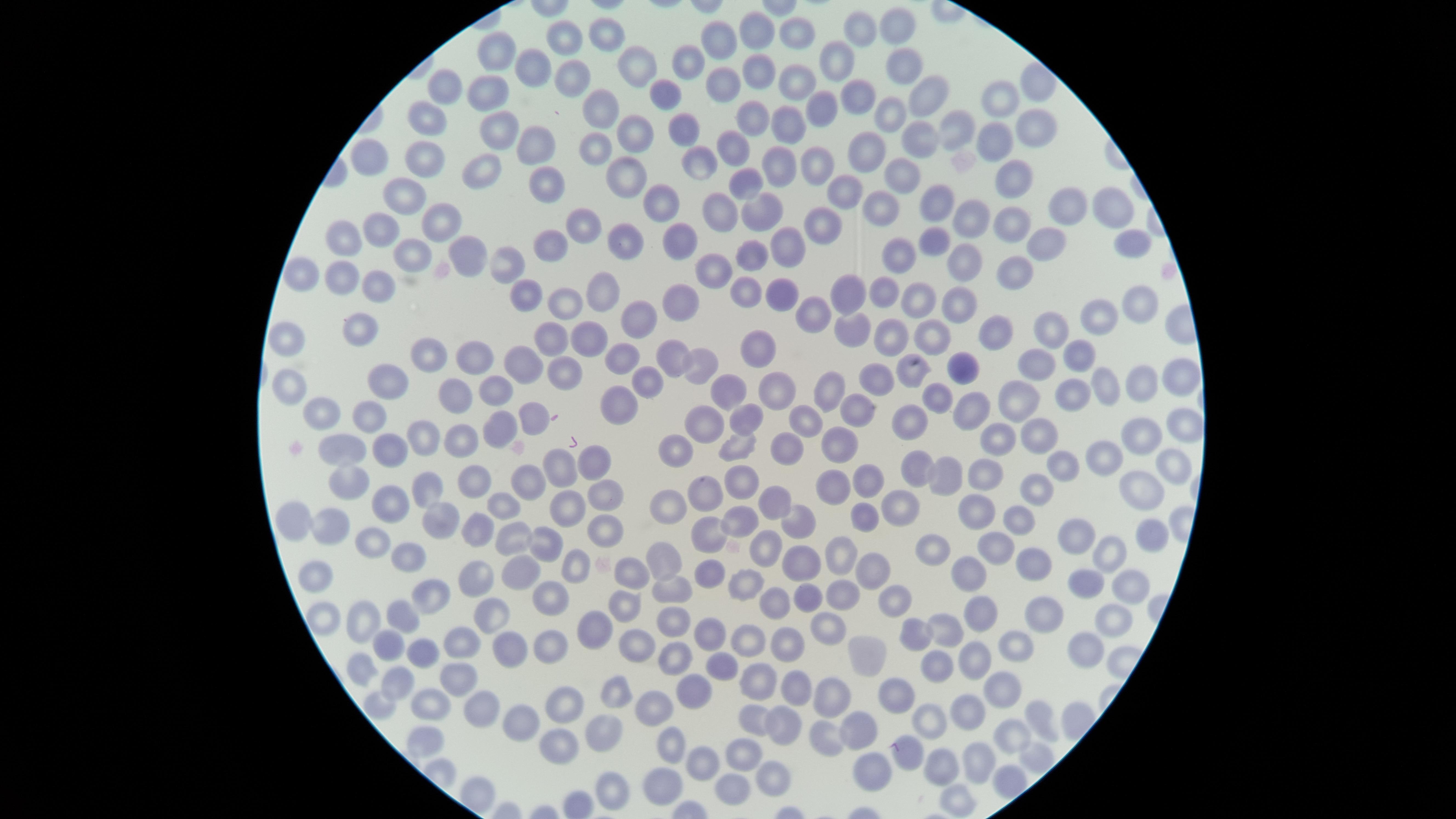
Approximate marker points as [x, y] in pixels.
Summary:
  - Uninfected RBCs: [861, 28], [901, 29], [608, 31], [800, 32], [755, 34], [567, 35], [721, 42], [500, 54], [691, 56], [838, 59], [642, 64], [900, 64], [531, 70], [758, 70], [569, 79], [799, 79], [721, 82], [452, 86], [492, 86], [931, 87], [664, 88], [855, 96], [1002, 103], [596, 108], [821, 111], [430, 116], [752, 118], [889, 118], [681, 125], [790, 125], [960, 126], [496, 128], [637, 130], [1033, 130], [918, 137], [532, 138], [593, 144], [1000, 144], [731, 145], [867, 154], [696, 155], [379, 156], [424, 156], [818, 160], [778, 165], [898, 169], [629, 174], [1009, 175], [486, 176], [548, 185], [744, 185], [851, 192], [402, 195], [661, 202], [715, 206], [879, 206], [1062, 206], [1111, 208], [758, 210], [930, 211], [443, 217], [584, 218], [973, 218], [388, 220], [819, 222], [1016, 224], [548, 237], [624, 237], [336, 240], [790, 241], [683, 244], [932, 246], [1048, 246], [1127, 247], [473, 249], [759, 252], [411, 261], [903, 261], [507, 263], [966, 264], [1017, 269], [709, 270], [304, 271], [375, 276], [344, 279], [601, 287], [783, 289], [747, 290], [885, 290], [563, 294], [530, 296], [917, 299], [683, 301], [851, 301], [963, 305], [1132, 305], [815, 316], [642, 319], [1105, 319], [893, 325], [854, 327], [989, 328], [1051, 330], [553, 331], [363, 332], [590, 334], [930, 337], [285, 341], [758, 347], [425, 348], [1080, 356], [476, 359], [521, 360], [676, 362], [622, 363], [701, 366], [561, 368], [1033, 368], [913, 372], [960, 372], [1175, 374], [878, 378], [1141, 383], [389, 384], [288, 386], [1109, 388], [645, 389], [495, 390], [780, 390], [1073, 391], [823, 392], [720, 396], [937, 398], [1019, 399], [451, 404], [617, 405], [324, 408], [968, 410], [855, 411], [372, 412], [523, 412], [912, 415], [747, 418], [806, 421], [699, 422], [498, 428], [1182, 428], [421, 430], [1040, 431], [1143, 438], [1002, 439], [737, 443], [346, 445], [840, 445], [456, 446], [790, 449], [394, 450], [677, 450], [1108, 453], [601, 460], [914, 465], [1168, 466], [1056, 467], [567, 468], [985, 469], [949, 477], [475, 480], [525, 481], [870, 481], [345, 482], [737, 486], [840, 488], [1031, 488], [1137, 488], [424, 491], [604, 492], [706, 492], [567, 500], [388, 501], [666, 503], [775, 504], [503, 505], [897, 507], [978, 509], [864, 512], [286, 517], [434, 519], [598, 519], [475, 520], [733, 520], [1017, 521], [330, 527], [800, 529], [509, 533], [1148, 535], [1071, 537], [370, 539], [707, 539], [543, 546], [841, 549], [927, 549], [995, 550], [764, 551], [403, 552], [1108, 553], [665, 561], [576, 562], [798, 563], [1030, 565], [873, 567], [978, 570], [316, 571], [514, 571], [632, 572], [709, 573], [475, 577], [1087, 579], [1128, 580], [746, 587], [669, 590], [843, 592], [429, 595], [549, 597], [813, 599], [779, 604], [896, 604], [625, 605], [1032, 605], [486, 612], [989, 614], [1111, 614], [401, 615], [671, 618], [324, 619], [835, 621], [364, 624], [591, 628], [949, 629], [712, 630], [911, 630], [748, 639], [784, 639], [1012, 642], [455, 644], [382, 645], [634, 645], [1084, 645], [507, 648], [556, 649], [417, 654], [681, 656], [874, 657], [979, 658], [934, 662], [722, 666], [351, 667], [754, 673], [450, 679], [393, 683], [613, 687], [795, 687], [693, 688], [1001, 690], [836, 691], [431, 697], [893, 697], [565, 701], [660, 703], [371, 707], [965, 714], [475, 715], [752, 717], [1034, 717], [517, 719], [931, 724], [776, 727], [861, 729], [607, 730], [827, 734], [1015, 735], [421, 737], [669, 743], [555, 746], [915, 747], [1036, 752], [742, 756], [980, 760], [943, 763], [699, 765], [868, 767], [768, 780], [668, 781], [733, 784], [610, 787], [955, 795]
  - Visible region: circular
  - Capture: smartphone photograph through the microscope eyepiece
  - Image size: 1456×819 pixels
  - Presence: no malaria parasites detected
  - Field of view: single
  - Preparation: thin blood film
  - Stain: Giemsa